Report the malaria status of this cell.
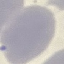
Uninfected.

capture = smartphone through the microscope eyepiece
image type = automatically extracted cell patch, resized to 64 × 64 pixels
preparation = thin smear
stain = Giemsa